Name the parasite shown.
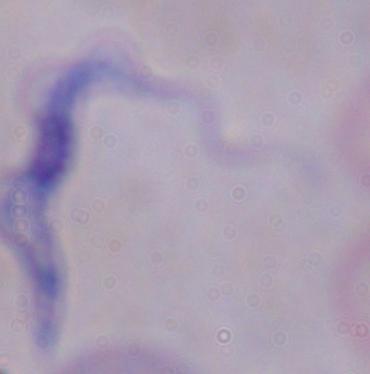

This is a trypanosome.

Photomicrograph. Captured at 1000x magnification.